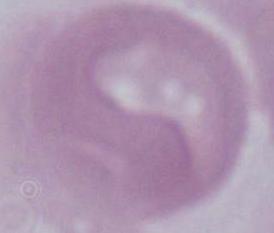 Photomicrograph. An erythrocyte is seen. Captured at 1000x magnification.